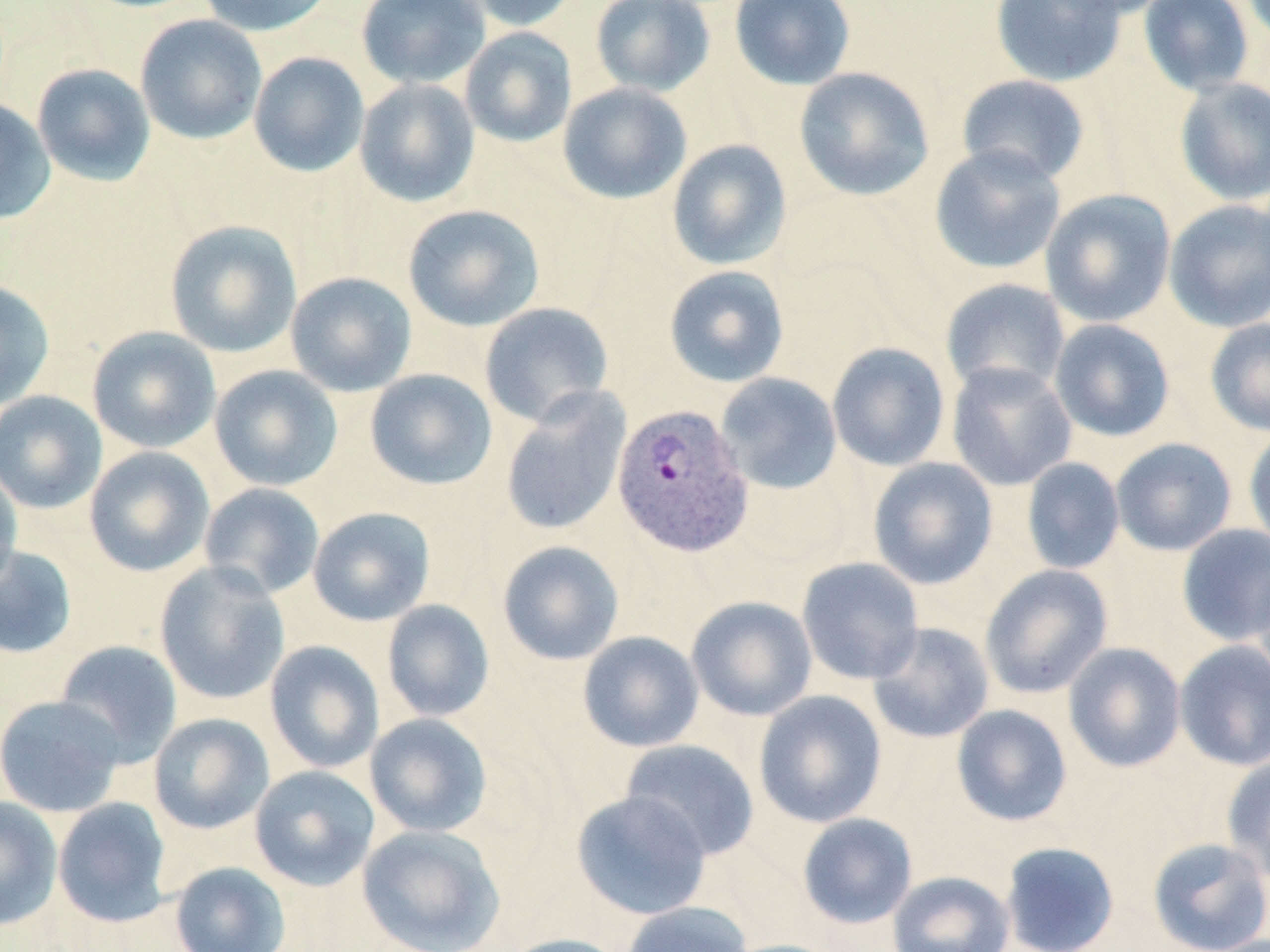
{
  "slide_level_diagnosis": "Plasmodium vivax",
  "preparation": "thin blood film",
  "magnification": "1000x",
  "uninfected_red_blood_cell_locations": "approximate bounding boxes as (x1,y1)-(x2,y2) corner pairs in pixels: (197,0)-(337,37), (356,0)-(491,89), (457,0)-(583,32), (590,0)-(715,97), (729,0)-(857,91), (990,0)-(1129,87), (1045,0)-(1174,18), (1137,0)-(1256,97), (135,14)-(267,145), (459,27)-(577,148), (248,51)-(369,177), (31,63)-(156,186), (794,67)-(935,202), (956,74)-(1091,186), (1174,77)-(1270,205), (354,79)-(480,207), (558,83)-(692,205), (0,97)-(56,225), (667,139)-(792,270), (929,144)-(1066,275), (1040,189)-(1176,327), (1163,199)-(1270,332), (403,204)-(544,332), (164,220)-(302,358), (664,265)-(790,388), (285,271)-(417,397), (940,278)-(1071,399), (0,280)-(55,411), (479,302)-(614,427), (1205,318)-(1270,437), (1049,319)-(1175,441), (87,326)-(221,453), (826,342)-(950,471), (946,361)-(1077,492), (209,365)-(343,492), (365,368)-(497,491), (714,372)-(842,495), (499,388)-(632,537), (0,391)-(107,514), (1243,427)-(1270,552), (1111,438)-(1237,556), (84,446)-(215,577), (867,457)-(999,590), (1021,458)-(1125,575), (0,467)-(22,590), (199,483)-(325,600), (308,507)-(435,626), (1177,524)-(1270,646), (497,540)-(625,666), (0,544)-(78,659), (796,557)-(925,685), (1249,557)-(1270,691), (154,561)-(290,704), (979,564)-(1113,698), (686,595)-(818,721), (382,600)-(495,721), (866,622)-(995,744), (578,631)-(704,752), (53,640)-(182,766), (264,640)-(384,773), (1173,640)-(1270,771), (1063,642)-(1186,773), (753,689)-(887,828), (0,694)-(124,817), (951,704)-(1073,827), (149,713)-(275,834), (364,713)-(492,837), (620,739)-(759,860), (1220,754)-(1270,884), (250,765)-(380,891), (571,790)-(712,920), (0,795)-(62,931), (52,797)-(172,927), (797,813)-(918,929), (357,824)-(506,952), (1147,837)-(1270,952), (1000,841)-(1119,952), (169,861)-(291,952), (887,870)-(1015,952), (620,902)-(754,952), (496,933)-(631,952), (718,938)-(848,952)",
  "plasmodium_vivax_infected_red_blood_cell_locations": "approximate bounding boxes as (x1,y1)-(x2,y2) corner pairs in pixels: (612,402)-(754,557)",
  "field_of_view": "single",
  "image_size": "1270×952 pixels",
  "stain": "May-Grünwald-Giemsa",
  "modality": "optical microscopy"
}